Describe the morphology of the erythrocytes.
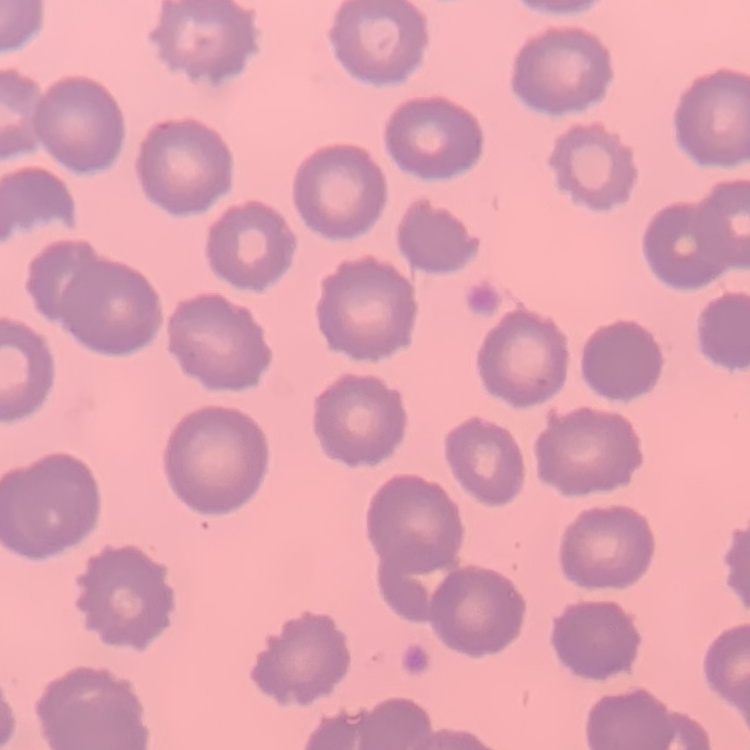

No rouleaux formation.

Thin peripheral smear. One tile cut from a larger photomicrograph. Stained with either Field's or Giemsa.